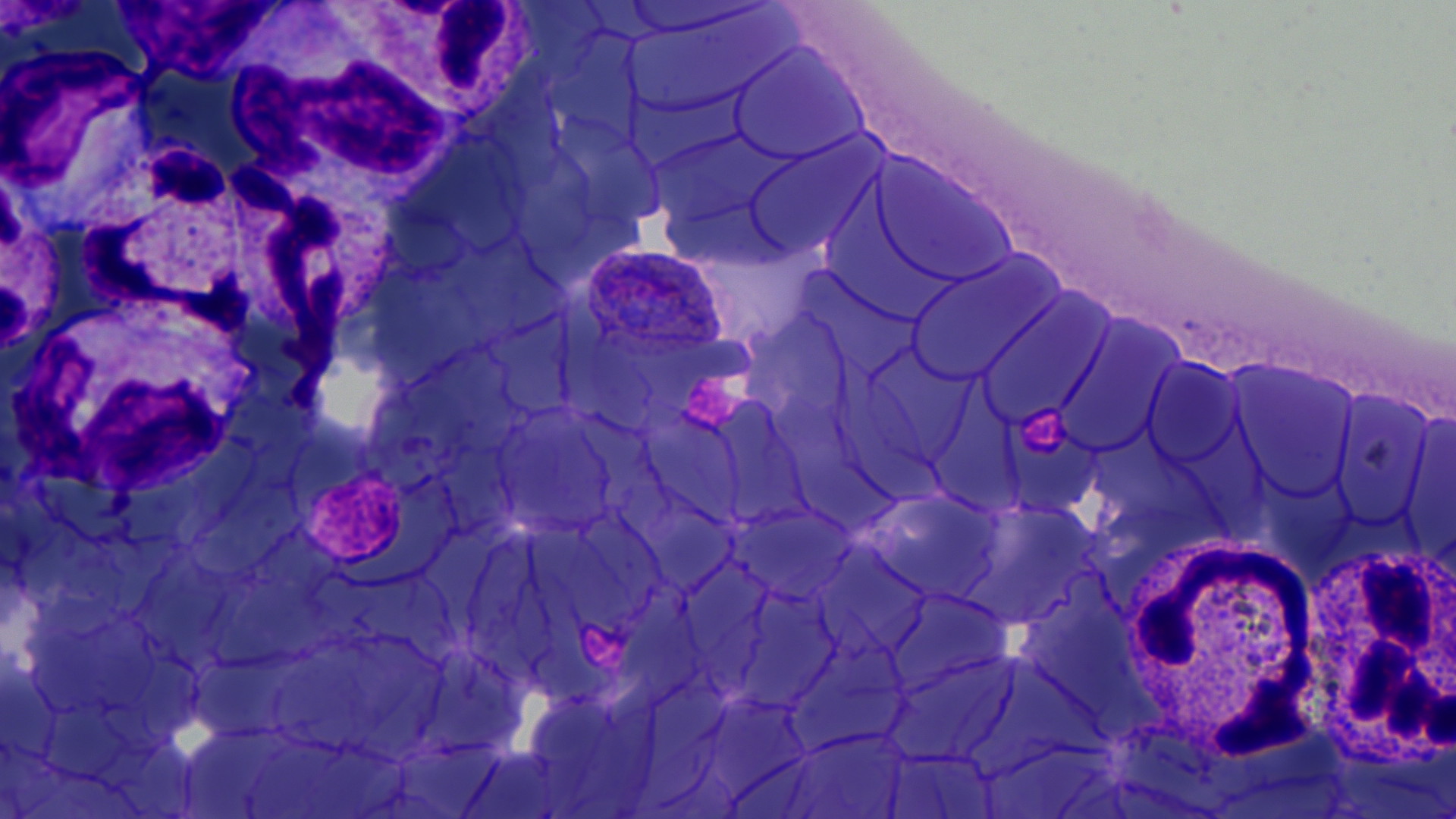 Approximate bounding boxes as named x1/y1/x2/y2 corners in pixels. White blood cell locations: (x1=220, y1=33, x2=465, y2=214), (x1=0, y1=40, x2=159, y2=244), (x1=64, y1=144, x2=251, y2=348), (x1=224, y1=156, x2=403, y2=358), (x1=10, y1=294, x2=256, y2=502), (x1=1315, y1=525, x2=1454, y2=781), (x1=1118, y1=534, x2=1322, y2=760). Uninfected red blood cell locations: (x1=627, y1=11, x2=793, y2=114), (x1=729, y1=45, x2=868, y2=166), (x1=648, y1=128, x2=785, y2=232), (x1=744, y1=140, x2=878, y2=258), (x1=864, y1=158, x2=1018, y2=290), (x1=906, y1=252, x2=1063, y2=388), (x1=973, y1=297, x2=1117, y2=428), (x1=1055, y1=325, x2=1180, y2=456), (x1=1142, y1=357, x2=1248, y2=468), (x1=1230, y1=364, x2=1359, y2=504), (x1=1330, y1=390, x2=1436, y2=527), (x1=494, y1=412, x2=618, y2=535), (x1=869, y1=491, x2=1000, y2=602), (x1=955, y1=502, x2=1092, y2=625), (x1=732, y1=504, x2=854, y2=603), (x1=883, y1=590, x2=1007, y2=695), (x1=888, y1=655, x2=1019, y2=766), (x1=781, y1=728, x2=913, y2=819), (x1=880, y1=749, x2=997, y2=816). Plasmodium ovale-infected red blood cell locations: (x1=581, y1=246, x2=730, y2=350). Slide-level diagnosis: Plasmodium ovale. Optical microscopy. Captured at 1000x magnification. Image is 1456×819 pixels. Thin blood film. May-Grünwald-Giemsa stain. One field of a larger specimen.